Classify this cell by malaria status.
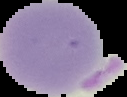

Uninfected.

image type = segmented cell region on a black background
preparation = thin blood smear
image size = 127×97 pixels